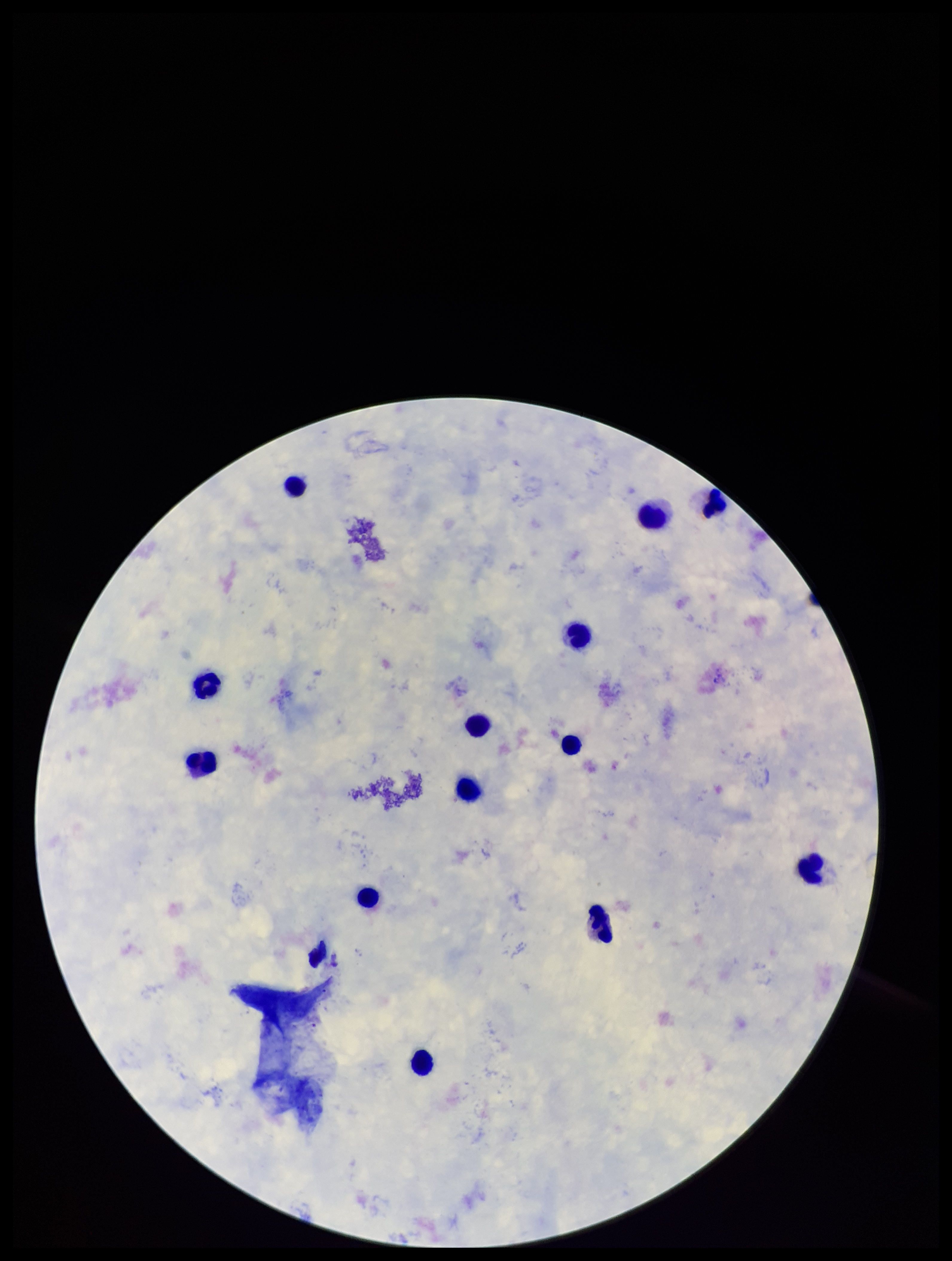 Plasmodium parasites: none identified. Leukocyte count: 13. Patient malaria status: negative. Image is 952×1261 pixels. Giemsa stain. Preparation: thick smear. Photographed through the microscope eyepiece with a smartphone camera. Parasite count: 0. Single field of view.